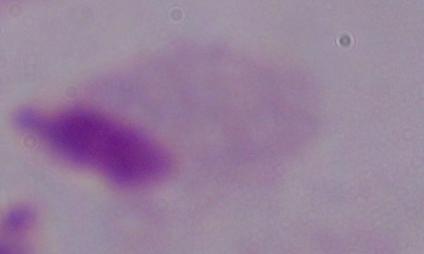

Photomicrograph. A trichomonad is seen. 1000x magnification.